State which cell type is depicted.
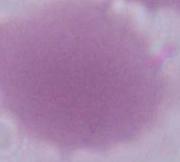

This is an erythrocyte.

modality: micrograph
magnification: 1000x